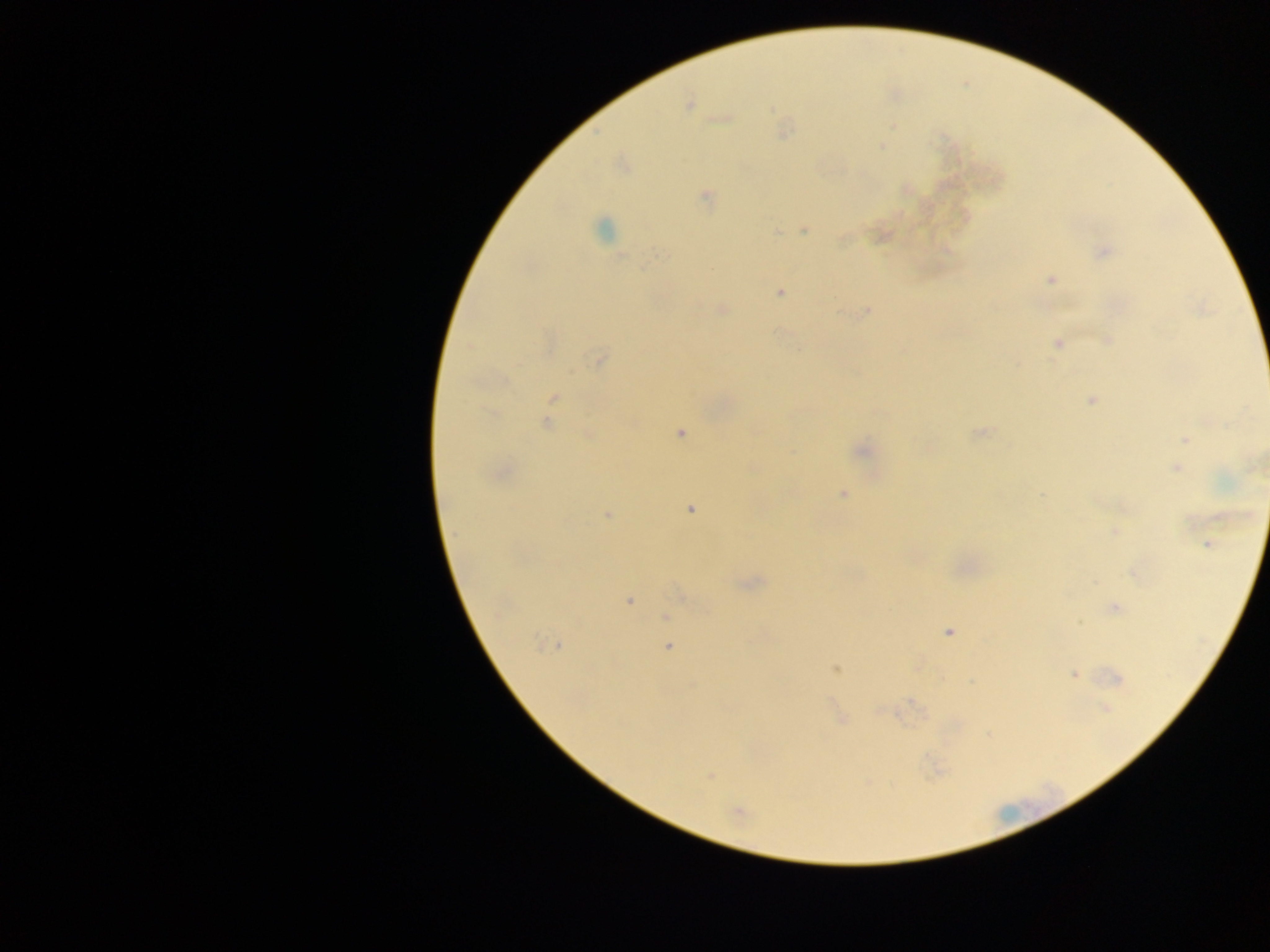 Approximate centers as {x, y} in pixels. Malaria parasite locations: {688, 106}, {882, 145}, {705, 197}, {603, 229}, {804, 230}, {777, 231}, {1103, 252}, {661, 254}, {621, 256}, {1050, 280}, {779, 294}, {721, 310}, {866, 312}, {1107, 340}, {1056, 343}, {599, 360}, {554, 397}, {1091, 400}, {547, 424}, {681, 433}, {979, 433}, {588, 435}, {1185, 440}, {861, 451}, {1176, 468}, {843, 494}, {1042, 496}, {690, 509}, {607, 515}, {1115, 532}, {1207, 544}, {1133, 573}, {629, 601}, {1115, 608}, {665, 617}, {1079, 623}, {948, 632}, {538, 642}, {557, 645}, {669, 647}, {837, 669}, {1073, 674}, {1116, 678}, {692, 684}, {1105, 707}, {709, 776}, {737, 811}. Thick blood smear. Single field of view. Sample from Ghana. Mobile-phone photograph taken through the microscope. Image is 1270×952 pixels.